Report the malaria status of this cell.
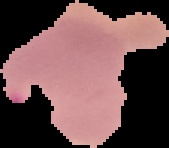

It is parasitized.

Summary:
  - Image type: cell region segmented out of the field of view; surrounding area masked to black
  - Image size: 169×148 pixels
  - Preparation: thin blood film